Name the parasite shown.
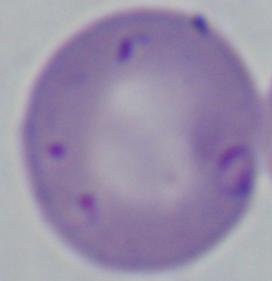
Babesia.

modality: photomicrograph
magnification: 1000x